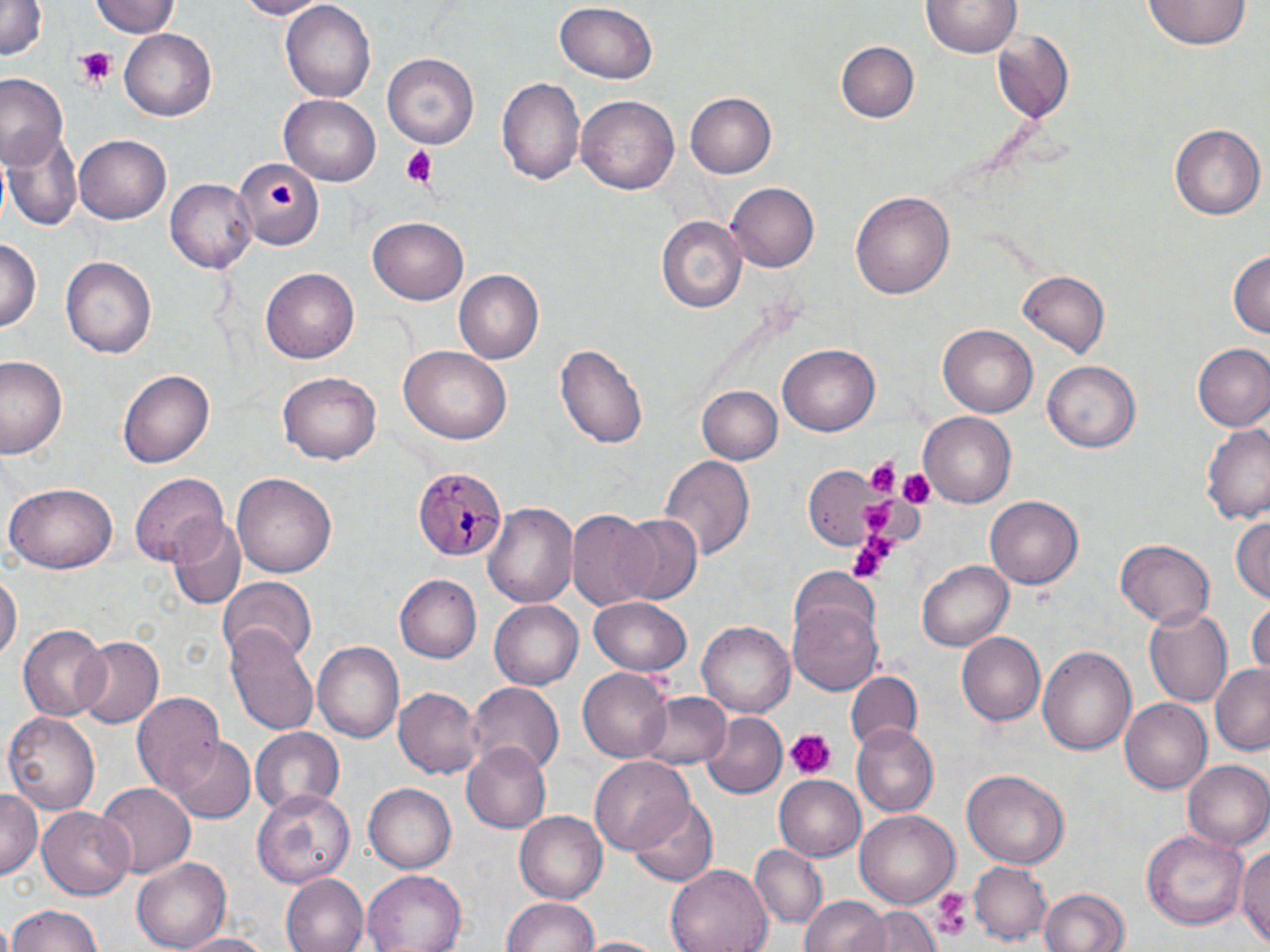
Approximate bounding boxes as (x1,y1)-(x2,y2) corner pairs in pixels. Plasmodium malariae-infected red blood cell locations: (414,468)-(507,563). Platelet locations: (74,47)-(116,89), (397,146)-(437,188), (267,180)-(301,210), (863,454)-(902,498), (893,466)-(935,508), (861,500)-(894,537), (847,532)-(895,583), (785,730)-(837,780), (933,889)-(973,941). Uninfected red blood cell locations: (91,0)-(178,39), (233,0)-(334,19), (918,0)-(1023,61), (1143,0)-(1251,50), (0,1)-(46,62), (281,2)-(375,102), (554,4)-(658,86), (118,30)-(216,120), (992,32)-(1075,120), (837,41)-(919,123), (383,52)-(481,149), (0,74)-(68,168), (496,78)-(586,186), (685,92)-(776,179), (576,94)-(679,192), (279,95)-(382,188), (1168,124)-(1263,221), (2,127)-(84,233), (72,135)-(170,224), (234,156)-(322,250), (166,179)-(257,271), (726,183)-(819,272), (851,190)-(955,301), (657,214)-(747,314), (369,217)-(468,304), (0,235)-(41,337), (1228,249)-(1269,342), (62,256)-(157,359), (261,267)-(359,364), (453,267)-(545,362), (1018,271)-(1110,355), (939,325)-(1036,417), (553,341)-(650,450), (1192,343)-(1270,433), (779,344)-(879,436), (397,346)-(510,445), (0,355)-(68,459), (1043,360)-(1138,451), (117,368)-(214,468), (279,369)-(382,465), (696,385)-(782,466), (918,413)-(1014,507), (1200,423)-(1270,525), (659,453)-(754,560), (130,472)-(232,566), (231,473)-(338,578), (3,484)-(119,573), (986,496)-(1083,590), (483,501)-(578,609), (567,510)-(659,613), (613,513)-(704,605), (1231,513)-(1270,603), (168,519)-(246,610), (1114,540)-(1214,628), (919,558)-(1014,649), (0,568)-(20,666), (394,575)-(481,664), (217,577)-(317,665), (788,596)-(882,697), (589,597)-(692,676), (488,600)-(584,691), (1249,600)-(1270,680), (1144,606)-(1234,707), (699,622)-(794,716), (18,624)-(109,722), (225,628)-(318,735), (958,632)-(1047,725), (73,636)-(163,729), (312,642)-(403,746), (1037,644)-(1136,757), (1211,661)-(1270,756), (578,670)-(670,761), (845,671)-(922,753), (467,681)-(562,771), (394,686)-(484,778), (634,690)-(729,768), (134,691)-(228,801), (1119,696)-(1211,791), (699,711)-(788,800), (4,712)-(101,812), (851,724)-(939,817), (249,730)-(345,818), (169,735)-(255,822), (463,741)-(554,833), (591,758)-(693,857), (1184,760)-(1270,851), (963,769)-(1070,868), (773,775)-(867,860), (94,782)-(193,877), (363,782)-(457,873), (253,789)-(356,887), (0,790)-(41,878), (625,793)-(718,886), (37,807)-(134,900), (856,809)-(959,906), (516,810)-(607,903), (1141,828)-(1247,929), (1238,840)-(1270,949), (748,844)-(827,930), (132,858)-(233,952), (968,861)-(1053,945), (667,863)-(772,952), (362,869)-(468,952), (279,874)-(369,952), (1035,884)-(1132,952), (799,894)-(891,952), (502,895)-(601,952), (5,904)-(101,952), (859,905)-(939,952), (175,932)-(278,952), (580,936)-(663,952). Slide-level diagnosis: Plasmodium malariae. Captured at 1000x magnification. Light microscopy. Single field of view. Image is 1270×952 pixels. Thin blood film. May-Grünwald-Giemsa stain.